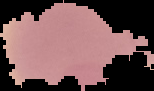
{
  "image_type": "segmented cell region on a black background",
  "result": "negative for malaria parasites",
  "image_size": "154×91 pixels",
  "preparation": "thin blood smear"
}